Identify the parasite.
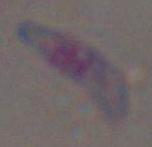

Toxoplasma gondii.

Summary:
  - Modality: photomicrograph
  - Magnification: 1000x